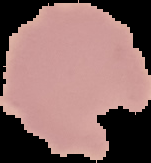

Summary:
  - Preparation: thin blood film
  - Image size: 151×163 pixels
  - Result: negative for malaria parasites
  - Image type: segmented cell region with the area outside set to black